Give the preparation type.
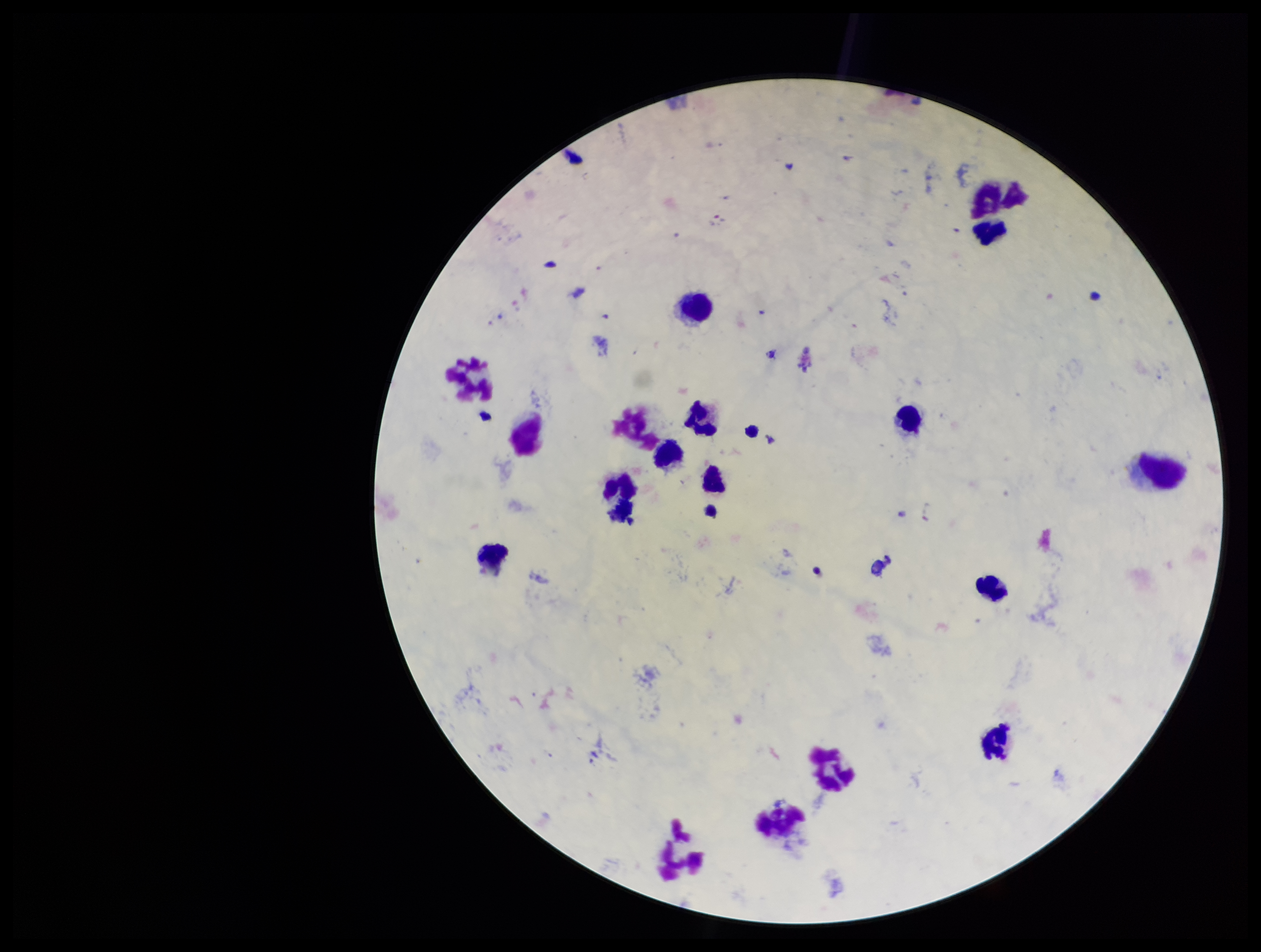

A thick smear.

Summary:
  - Stain: Giemsa
  - Image size: 1261×952 pixels
  - Capture: smartphone photograph through the microscope eyepiece
  - Species reported for this patient: Plasmodium vivax
  - Plasmodium parasites: none seen
  - Field of view: one from this slide
  - Leukocyte count: 17
  - Parasite count: 0
  - Patient malaria status: infected